Locate every uninfected red blood cell.
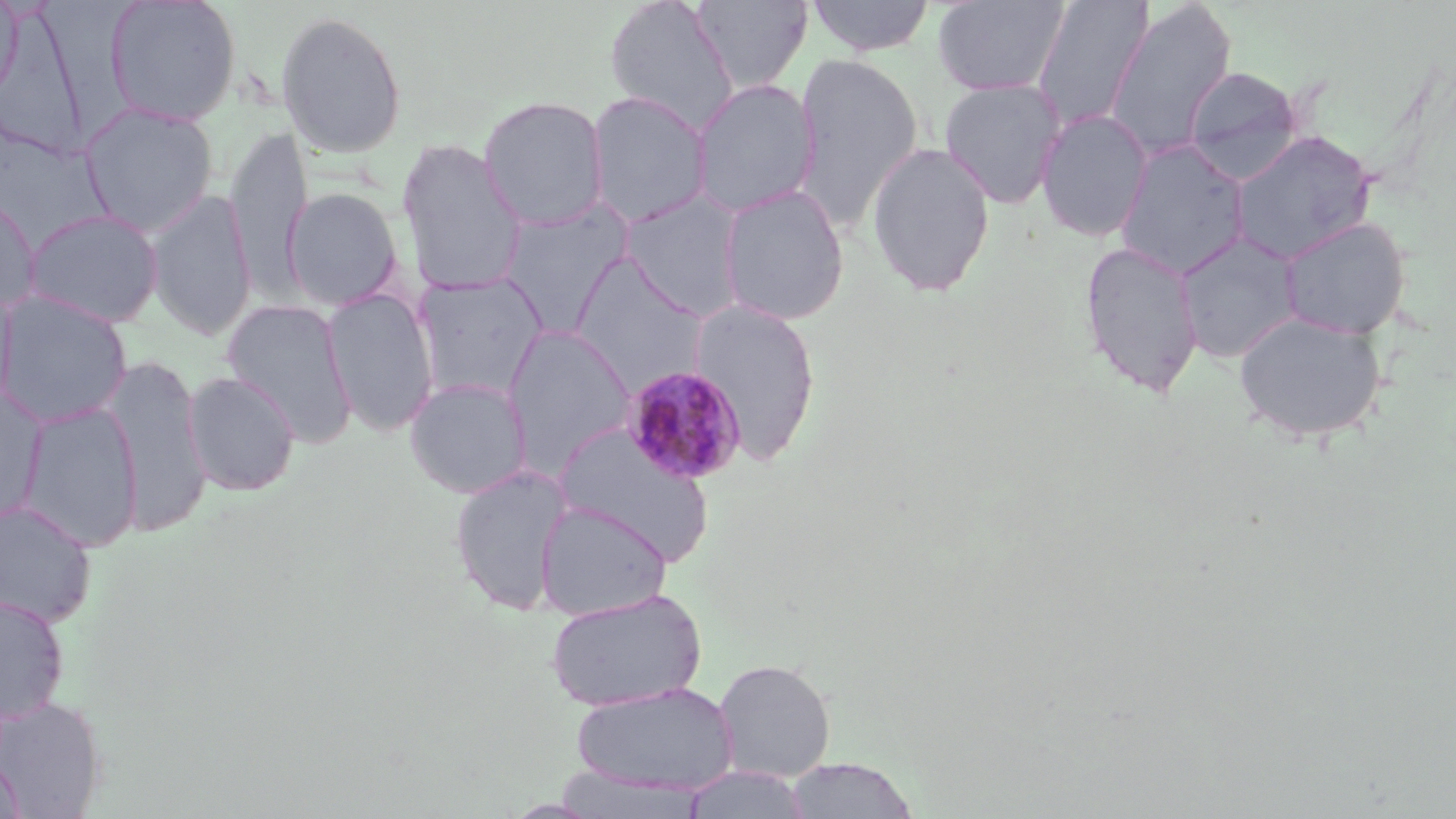

Approximate bounding boxes as named x1/y1/x2/y2 corners in pixels.
Uninfected red blood cells: (x1=0, y1=0, x2=23, y2=107), (x1=105, y1=0, x2=242, y2=127), (x1=603, y1=0, x2=740, y2=134), (x1=691, y1=0, x2=814, y2=93), (x1=805, y1=0, x2=936, y2=56), (x1=932, y1=0, x2=1071, y2=97), (x1=1031, y1=0, x2=1156, y2=132), (x1=1104, y1=2, x2=1237, y2=161), (x1=0, y1=5, x2=93, y2=160), (x1=274, y1=9, x2=408, y2=160), (x1=793, y1=53, x2=923, y2=232), (x1=1182, y1=64, x2=1304, y2=180), (x1=690, y1=78, x2=820, y2=217), (x1=938, y1=78, x2=1067, y2=209), (x1=586, y1=91, x2=712, y2=228), (x1=477, y1=95, x2=610, y2=231), (x1=79, y1=102, x2=219, y2=236), (x1=1036, y1=108, x2=1153, y2=242), (x1=225, y1=125, x2=311, y2=299), (x1=1228, y1=130, x2=1377, y2=265), (x1=395, y1=137, x2=528, y2=297), (x1=1115, y1=139, x2=1251, y2=279), (x1=865, y1=141, x2=996, y2=297), (x1=717, y1=184, x2=850, y2=325), (x1=282, y1=186, x2=404, y2=312), (x1=146, y1=189, x2=256, y2=342), (x1=618, y1=190, x2=745, y2=320), (x1=0, y1=192, x2=41, y2=314), (x1=496, y1=200, x2=635, y2=336), (x1=23, y1=209, x2=164, y2=328), (x1=1278, y1=216, x2=1411, y2=340), (x1=1174, y1=231, x2=1303, y2=363), (x1=1078, y1=239, x2=1204, y2=400), (x1=569, y1=254, x2=709, y2=394), (x1=413, y1=272, x2=548, y2=403), (x1=0, y1=281, x2=19, y2=418), (x1=323, y1=286, x2=439, y2=436), (x1=0, y1=290, x2=132, y2=427), (x1=688, y1=297, x2=822, y2=466), (x1=221, y1=298, x2=358, y2=447), (x1=1232, y1=310, x2=1389, y2=444), (x1=502, y1=324, x2=637, y2=477), (x1=104, y1=353, x2=212, y2=537), (x1=183, y1=370, x2=301, y2=497), (x1=404, y1=377, x2=532, y2=498), (x1=0, y1=388, x2=47, y2=523), (x1=17, y1=401, x2=142, y2=552), (x1=553, y1=422, x2=717, y2=566), (x1=448, y1=464, x2=574, y2=616), (x1=0, y1=500, x2=98, y2=627), (x1=535, y1=501, x2=672, y2=618), (x1=546, y1=588, x2=706, y2=711), (x1=0, y1=594, x2=70, y2=724), (x1=713, y1=659, x2=836, y2=781), (x1=571, y1=681, x2=739, y2=795), (x1=0, y1=696, x2=107, y2=817), (x1=1, y1=754, x2=26, y2=819), (x1=784, y1=757, x2=919, y2=819), (x1=680, y1=766, x2=813, y2=819).

Plasmodium malariae-infected red blood cell locations: (x1=622, y1=365, x2=748, y2=484). Slide-level diagnosis: Plasmodium malariae. Image is 1456×819 pixels. Light microscopy. Single field of view. May-Grünwald-Giemsa stain. Thin blood film. 1000x magnification.